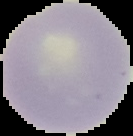

preparation = thin blood film
malaria status = uninfected
image type = cell region segmented out of the field of view; surrounding area masked to black
image size = 133×136 pixels